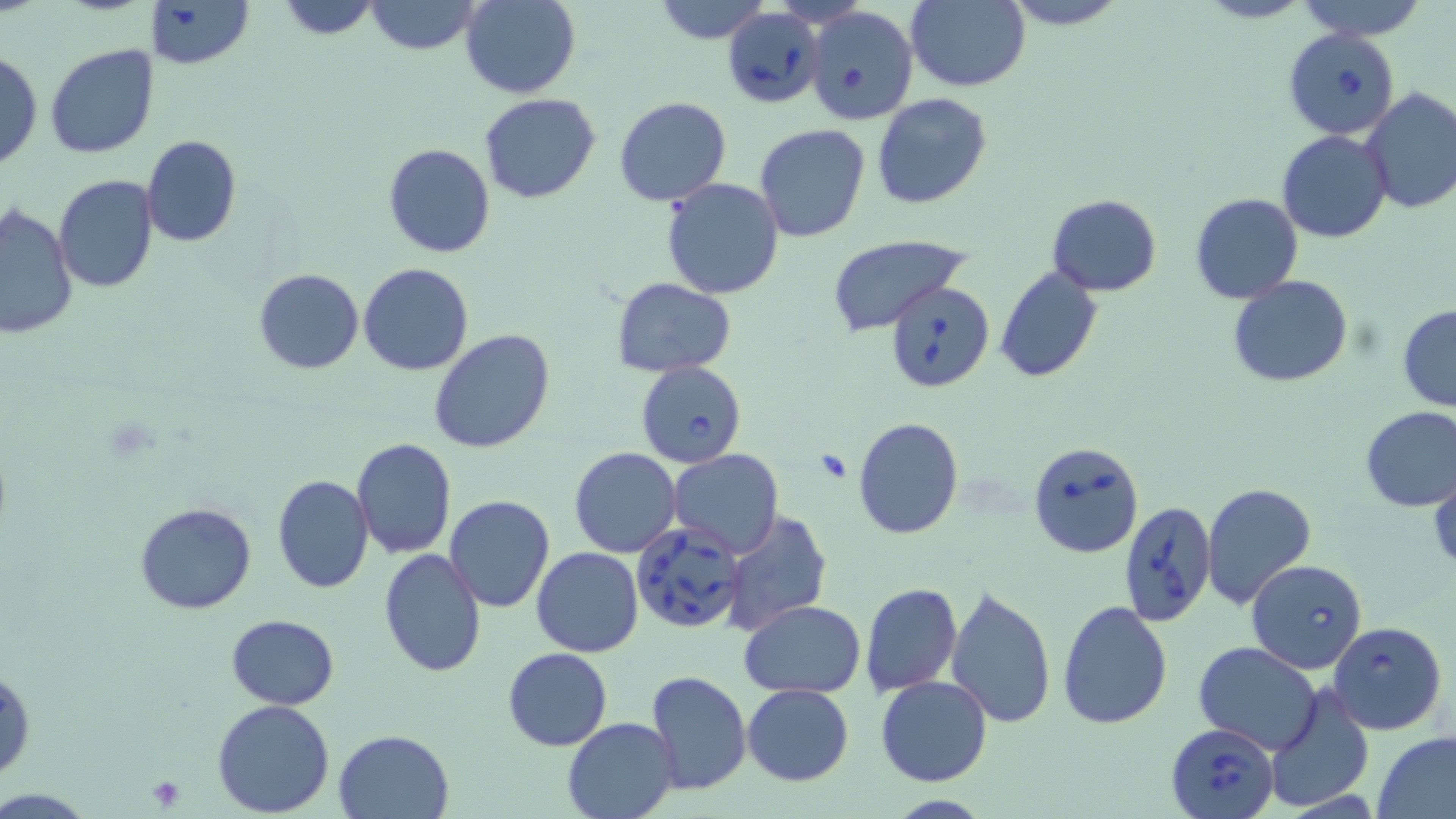
slide-level diagnosis = Babesia divergens
stain = May-Grünwald-Giemsa
platelet locations = approximate bounding boxes as (x1,y1)-(x2,y2) corner pairs in pixels: (146,775)-(188,811)
Babesia divergens-infected red blood cell locations = approximate bounding boxes as (x1,y1)-(x2,y2) corner pairs in pixels: (724,8)-(825,109), (1284,29)-(1402,139), (885,281)-(995,393), (635,362)-(746,468), (1027,440)-(1144,559), (1118,499)-(1215,630), (631,523)-(747,635), (1247,558)-(1367,673), (1328,620)-(1448,736), (1168,721)-(1280,819)
image size = 1456×819 pixels
preparation = thin blood smear
magnification = 1000x
field of view = one of a larger specimen
modality = light microscopy
uninfected red blood cell locations = approximate bounding boxes as (x1,y1)-(x2,y2) corner pairs in pixels: (141,0)-(254,69), (276,0)-(381,39), (365,0)-(481,55), (461,0)-(580,99), (648,0)-(775,43), (998,0)-(1133,30), (1193,0)-(1318,24), (1294,0)-(1433,40), (903,1)-(1031,91), (804,6)-(918,125), (45,45)-(159,160), (0,49)-(42,173), (1360,89)-(1456,214), (479,93)-(601,204), (871,93)-(992,209), (613,97)-(731,206), (755,124)-(870,242), (1277,130)-(1392,243), (141,135)-(240,249), (383,143)-(495,258), (53,174)-(158,292), (661,177)-(784,300), (1190,193)-(1303,304), (1046,194)-(1162,296), (1,204)-(76,339), (826,233)-(969,333), (358,262)-(475,377), (995,266)-(1102,383), (253,268)-(364,375), (1228,275)-(1353,388), (612,276)-(736,378), (1396,304)-(1456,412), (428,329)-(555,455), (1359,405)-(1456,512), (851,416)-(963,540), (351,438)-(457,559), (569,448)-(681,557), (667,450)-(784,558), (1428,467)-(1456,574), (273,474)-(373,593), (1202,482)-(1318,612), (443,495)-(555,612), (135,502)-(257,615), (719,508)-(832,636), (531,547)-(643,657), (378,549)-(487,679), (861,582)-(962,697), (945,583)-(1059,727), (739,600)-(866,698), (1057,600)-(1173,730), (226,614)-(338,708), (1193,641)-(1321,753), (503,647)-(612,750), (0,667)-(35,784), (644,670)-(752,795), (876,674)-(993,787), (741,683)-(853,785), (1263,683)-(1376,813), (212,699)-(335,818), (561,716)-(680,819), (334,729)-(455,819), (1372,732)-(1456,819)